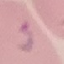 Result: malaria parasites identified. Photographed with a smartphone camera at the microscope eyepiece. Automatically extracted cell patch, resized to 64 × 64 pixels. Thin blood film. Giemsa stain.